Classify this cell by malaria status.
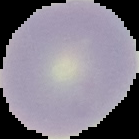

Uninfected.

preparation: thin blood smear
image_size: 139×139 pixels
image_type: segmented cell region with the area outside set to black